State the blood parasite species.
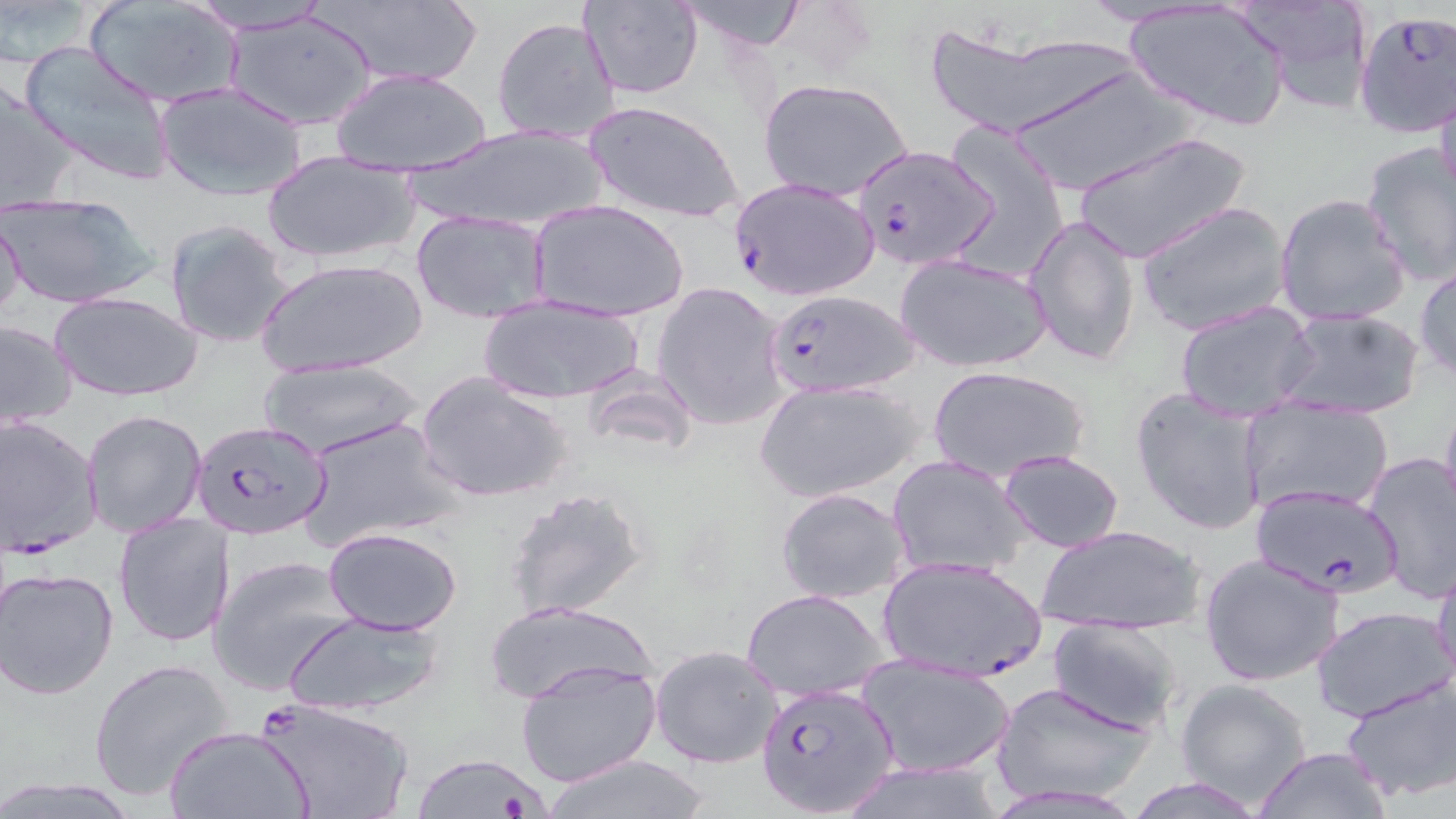
Plasmodium falciparum.

Summary:
  - Coordinate format: approximate bounding boxes as (x1,y1)-(x2,y2) corner pairs in pixels
  - Plasmodium falciparum-infected red blood cell locations: (1352,10)-(1456,139), (854,145)-(999,271), (729,176)-(881,302), (762,290)-(921,399), (188,413)-(337,541), (1,414)-(102,556), (1247,483)-(1403,600), (879,555)-(1048,684), (759,681)-(901,816), (252,696)-(410,818)
  - Uninfected red blood cell locations: (176,0)-(340,33), (311,0)-(485,89), (675,0)-(813,52), (580,1)-(703,99), (1238,1)-(1374,113), (87,2)-(242,108), (1124,2)-(1290,130), (221,8)-(381,129), (491,16)-(621,144), (925,30)-(1130,138), (18,40)-(177,187), (1005,66)-(1191,195), (332,67)-(492,177), (759,78)-(913,202), (0,82)-(80,214), (154,82)-(309,200), (1433,82)-(1455,204), (584,99)-(744,226), (403,123)-(612,235), (944,130)-(1070,277), (1072,131)-(1250,265), (1359,141)-(1456,286), (262,152)-(419,265), (0,191)-(160,310), (1275,192)-(1411,328), (532,198)-(688,321), (1135,201)-(1290,336), (409,210)-(555,324), (1023,213)-(1141,369), (0,215)-(28,323), (162,218)-(295,348), (895,252)-(1052,373), (256,257)-(428,378), (1415,259)-(1456,382), (651,281)-(788,431), (50,291)-(203,402), (475,296)-(646,406), (1175,300)-(1318,419), (1274,306)-(1424,420), (0,320)-(79,428), (257,359)-(421,459), (927,366)-(1089,482), (580,369)-(700,463), (416,372)-(575,503), (755,377)-(924,502), (1130,388)-(1268,537), (1438,391)-(1456,527), (1240,398)-(1394,515), (80,410)-(208,539), (298,415)-(461,553), (997,449)-(1125,553), (1361,452)-(1456,604), (887,455)-(1030,579), (502,484)-(651,622), (775,487)-(912,604), (113,511)-(236,648), (1035,523)-(1205,637), (322,526)-(463,636), (1199,552)-(1348,688), (1431,553)-(1456,690), (208,554)-(359,697), (1,566)-(120,700), (741,589)-(889,701), (487,600)-(654,706), (1311,605)-(1453,721), (283,609)-(449,717), (1046,618)-(1185,734), (649,644)-(784,769), (855,655)-(1013,777), (516,657)-(660,787), (89,658)-(235,803), (1341,673)-(1456,804), (993,679)-(1155,804), (1175,679)-(1314,807), (164,725)-(315,819), (1254,747)-(1389,819), (410,752)-(549,818), (539,752)-(714,818), (832,761)-(1008,818)
  - Platelet locations: (497,790)-(536,818)
  - Preparation: thin blood smear
  - Modality: light microscopy
  - Field of view: single
  - Stain: May-Grünwald-Giemsa
  - Magnification: 1000x
  - Image size: 1456×819 pixels